State the blood parasite species.
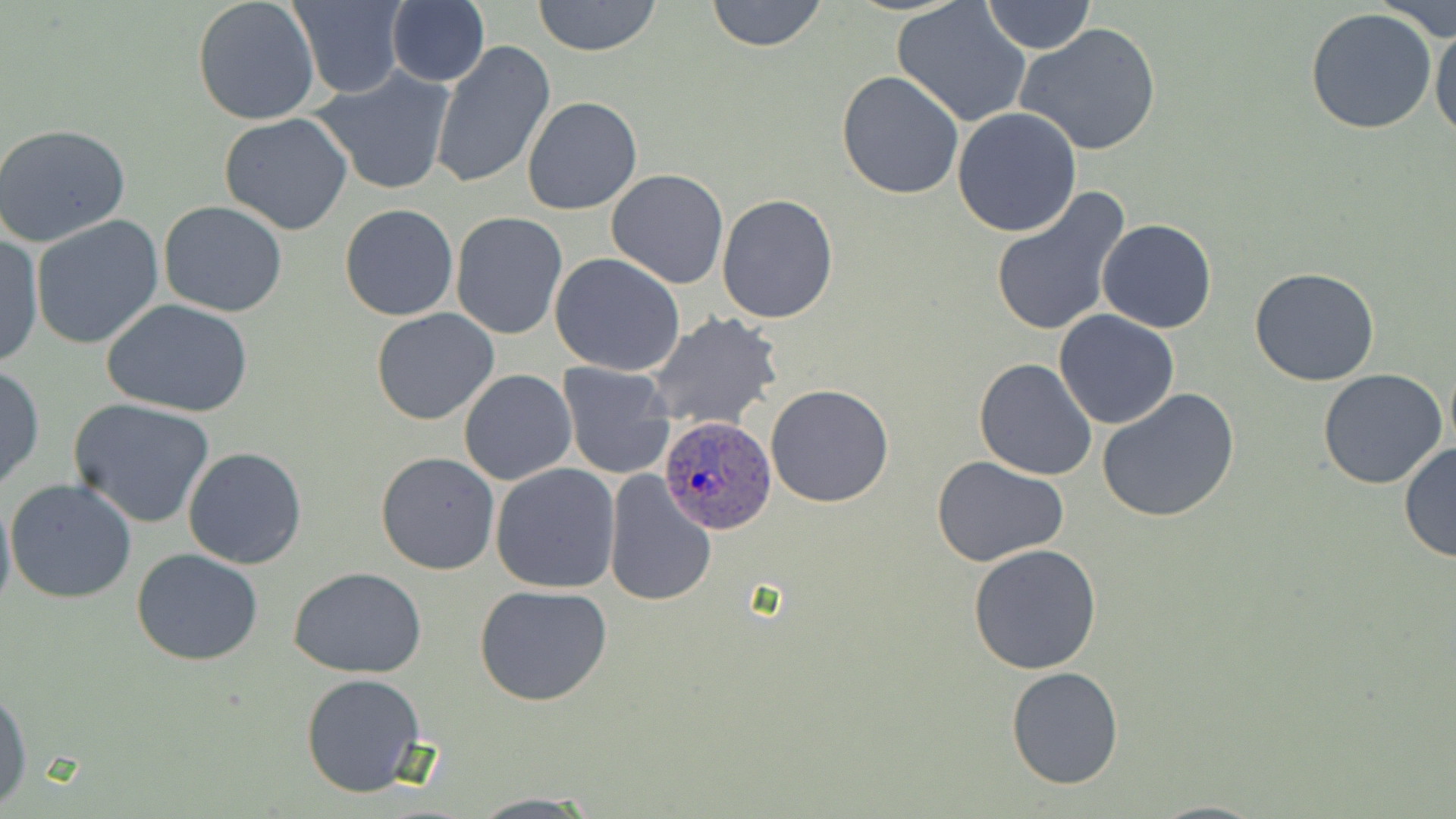
Plasmodium ovale.

Approximate bounding boxes as [x1, y1, x2, y2] in pixels. Plasmodium ovale-infected red blood cell locations: [657, 414, 777, 535]. Uninfected red blood cell locations: [192, 0, 320, 125], [288, 0, 406, 99], [386, 0, 490, 87], [531, 0, 663, 56], [705, 0, 828, 51], [981, 0, 1096, 54], [1376, 0, 1456, 45], [893, 3, 1032, 127], [1305, 7, 1437, 135], [1430, 14, 1456, 145], [1016, 21, 1162, 156], [431, 41, 555, 190], [313, 66, 457, 196], [836, 70, 964, 198], [521, 95, 644, 214], [952, 108, 1082, 237], [219, 113, 353, 236], [0, 124, 131, 245], [605, 169, 730, 290], [988, 185, 1132, 337], [716, 193, 839, 324], [158, 201, 289, 318], [339, 203, 460, 321], [450, 211, 567, 340], [32, 215, 165, 350], [1097, 219, 1218, 333], [1, 234, 43, 370], [549, 253, 686, 377], [1249, 267, 1381, 386], [102, 299, 255, 418], [370, 309, 499, 426], [1054, 309, 1180, 429], [646, 312, 784, 430], [973, 357, 1098, 481], [557, 362, 675, 481], [0, 364, 45, 491], [1317, 368, 1448, 489], [459, 369, 578, 484], [765, 384, 894, 508], [1096, 385, 1242, 523], [69, 399, 216, 528], [1398, 442, 1456, 563], [182, 446, 307, 570], [375, 452, 500, 575], [933, 456, 1070, 568], [490, 463, 621, 593], [605, 472, 717, 606], [5, 478, 137, 604], [0, 489, 16, 617], [968, 544, 1102, 675], [132, 548, 263, 665], [288, 567, 428, 677], [473, 583, 614, 707], [1006, 667, 1124, 788], [300, 672, 426, 797], [0, 685, 32, 808], [464, 794, 606, 817]. May-Grünwald-Giemsa stain. 1000x magnification. Optical microscopy. Thin blood film. One field of a larger specimen. Image is 1456×819 pixels.